Name the parasite shown.
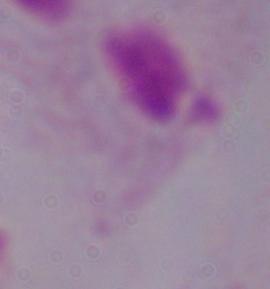
This is a trichomonad.

modality: micrograph
magnification: 1000x